Evaluate for parasitized red blood cells.
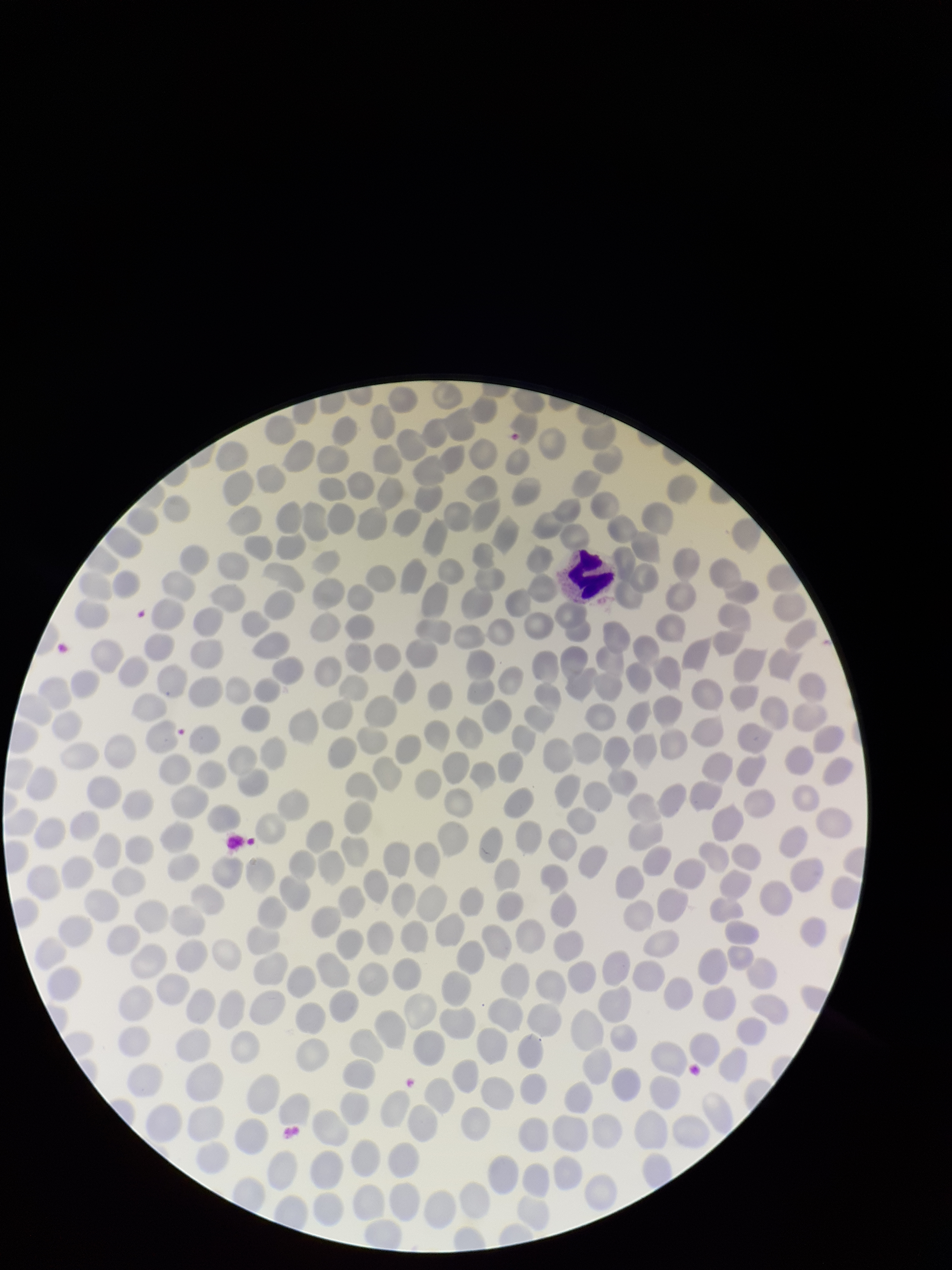
None detected.

Summary:
  - Species reported for this patient: Plasmodium falciparum
  - Field of view: single
  - Preparation: thin blood smear
  - Red blood cell count: 276
  - Patient malaria status: positive
  - Stain: Giemsa
  - Image size: 952×1270 pixels
  - Parasitized red blood cell count: 0
  - Capture: smartphone photograph through the microscope eyepiece